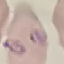
{
  "result": "malaria parasites detected",
  "image_type": "cell patch, automatically extracted from a larger field of view and resized to 64 × 64 pixels",
  "preparation": "thin blood smear",
  "stain": "Giemsa",
  "capture": "smartphone through the microscope eyepiece"
}